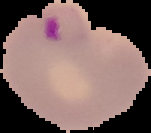

image size = 151×133 pixels
image type = segmented cell region with the area outside set to black
preparation = thin blood smear
malaria status = parasitized